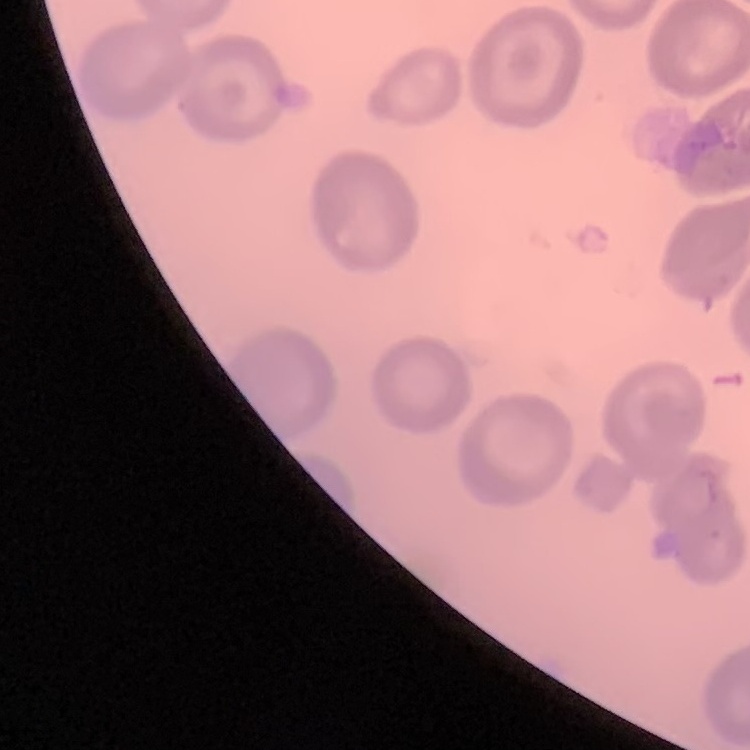
erythrocyte morphology = no rouleaux formation
preparation = thin blood smear
stain = Field's or Giemsa
image type = one tile cut from a larger photomicrograph